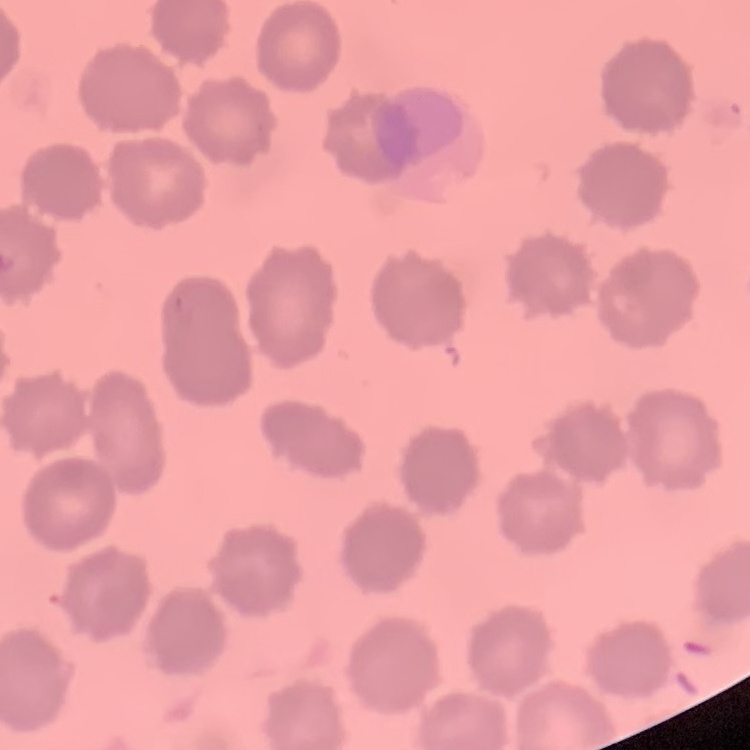
The red blood cells show no rouleaux formation. Thin blood film. Square crop of a larger photomicrograph. Stained with either Field's or Giemsa.